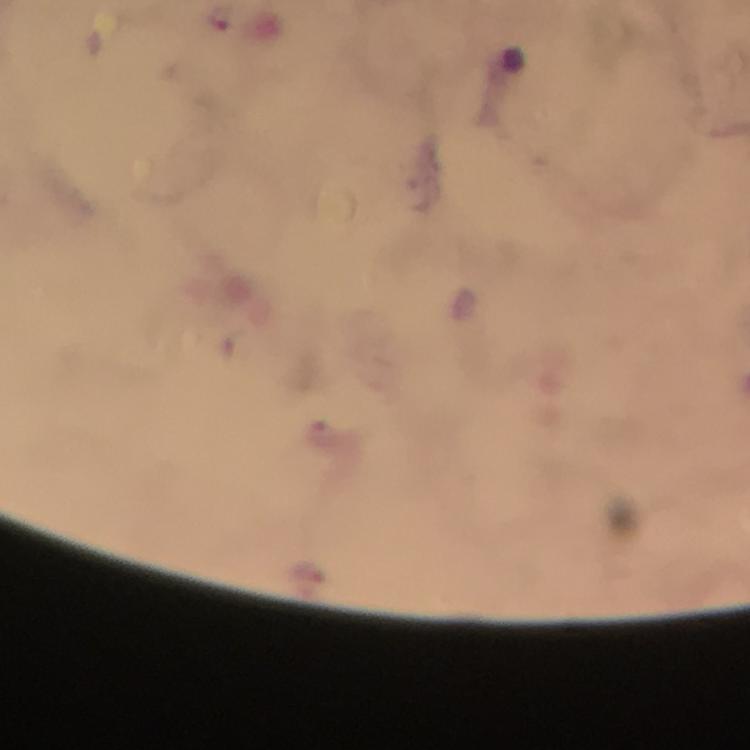

capture = smartphone mounted on the microscope
stain = Giemsa
image size = 750×750 pixels
preparation = thick blood smear
context = from a diagnostic examination for malaria
immersion oil = used
cropped from = one field of view
magnification = 100x
malaria parasite locations = approximate object centers, in pixels from the top-left corner: (x=221, y=19)